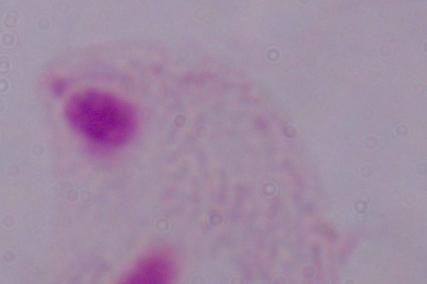

A trichomonad is shown. 1000x magnification. Micrograph.